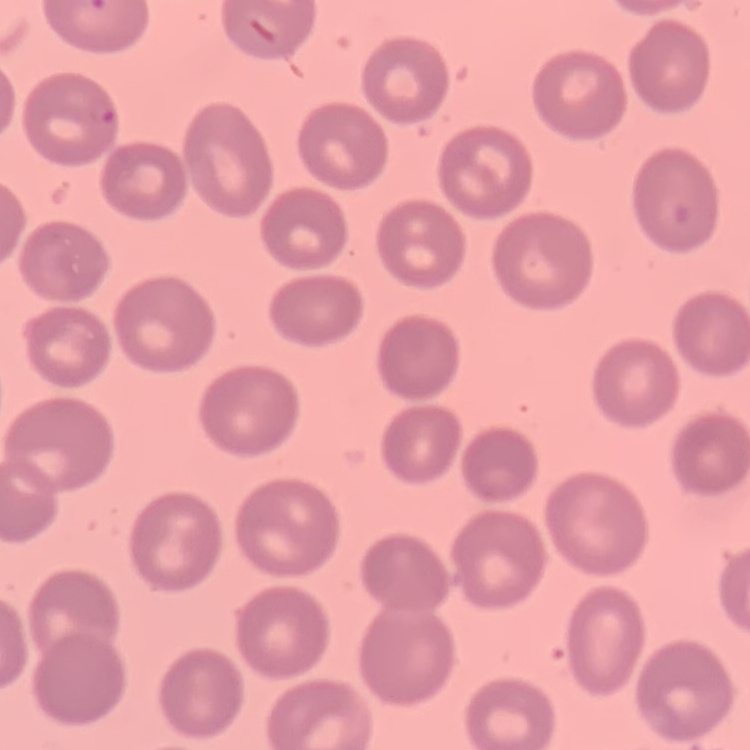
red_blood_cell_morphology: no rouleaux formation
image_type: one tile cut from a larger photomicrograph
stain: Field's or Giemsa
preparation: thin peripheral smear